Describe the morphology of the erythrocytes.
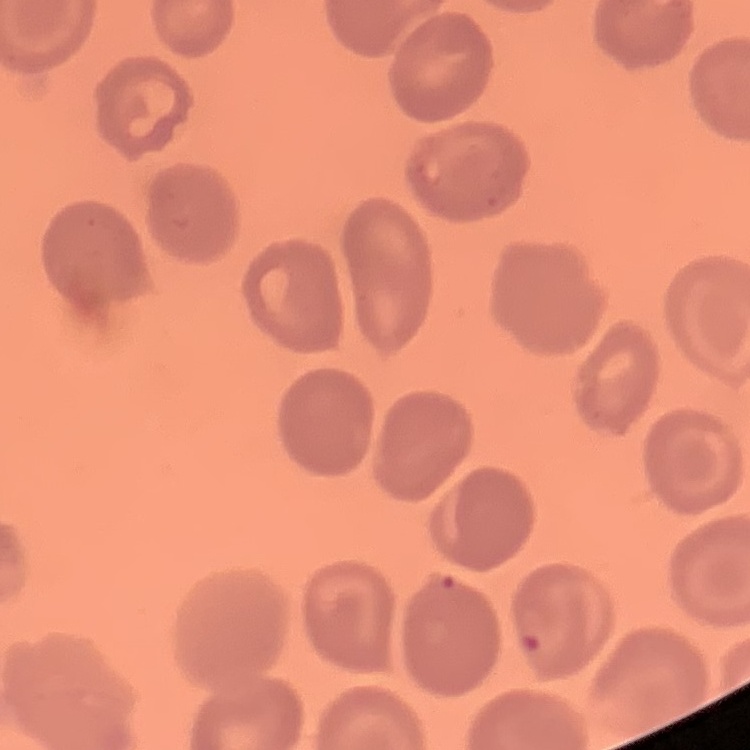
No rouleaux formation.

preparation = thin blood film
stain = Field's or Giemsa
image type = square crop of a larger photomicrograph